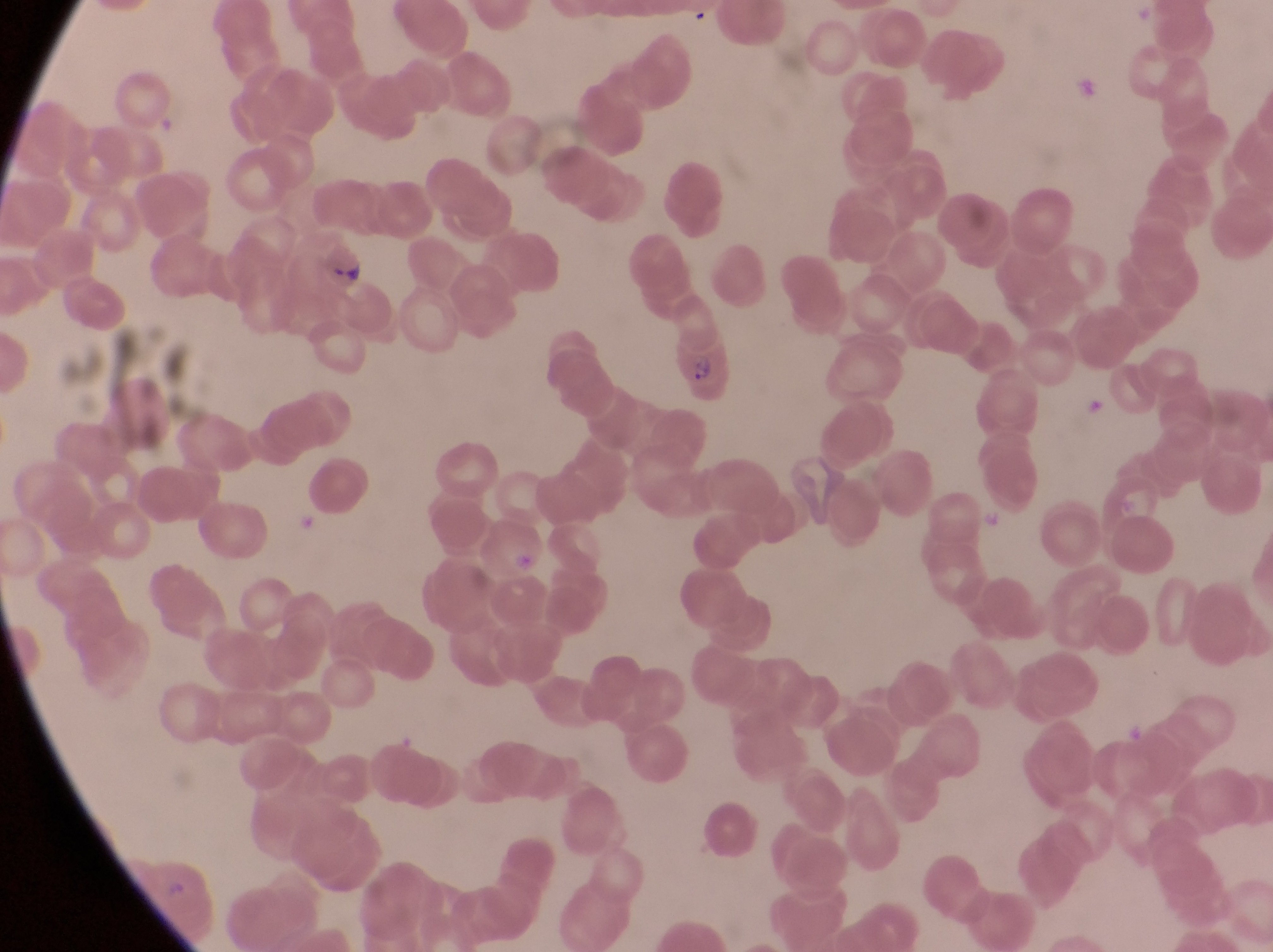

field of view = single
artifact (platelet-like body, stain precipitate, or debris) locations = approximate bounding boxes as [left, top, right, bottom] in pixels: [479, 517, 553, 585]
image size = 1273×952 pixels
parasitised red blood cell locations = approximate bounding boxes as [left, top, right, bottom] in pixels: [671, 337, 740, 402]
magnification = 1000x
country = Uganda
preparation = thin blood film
capture = smartphone photograph through the eyepiece of an Olympus CX-23 microscope